Identify the parasite.
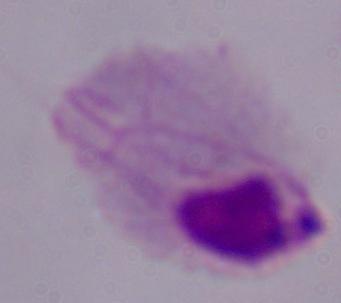
A trichomonad.

Photomicrograph. Captured at 1000x magnification.